Identify the parasite.
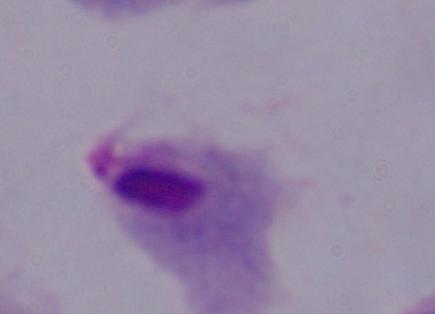
A trichomonad.

Summary:
  - Magnification: 1000x
  - Modality: photomicrograph